Report the malaria status of this cell.
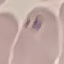

It is parasitized.

stain = Giemsa
preparation = thin blood film
capture = smartphone through the microscope eyepiece
image type = automatically extracted cell patch, resized to 64 × 64 pixels